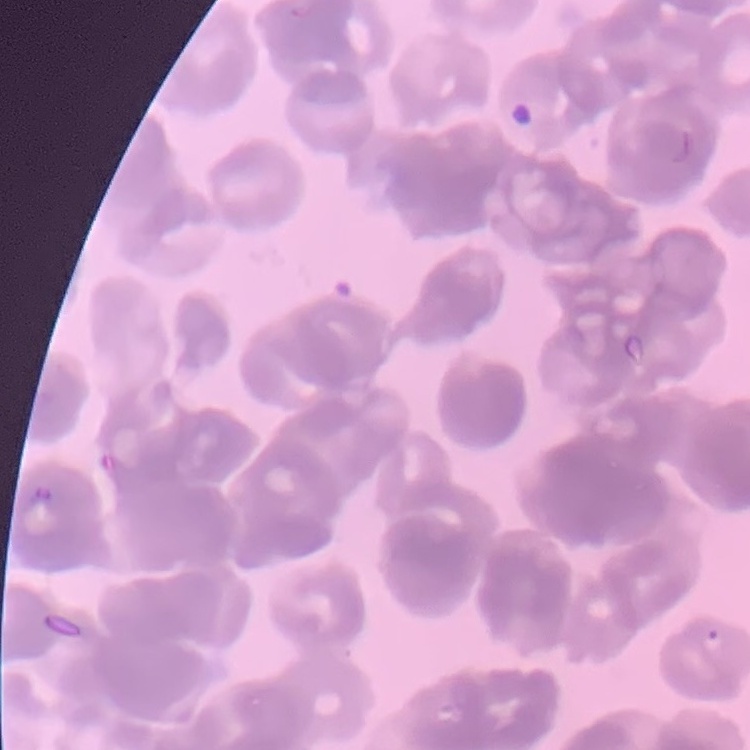
The erythrocytes exhibit rouleaux formation. Thin peripheral smear. Field's or Giemsa stain. Square crop of a larger photomicrograph.